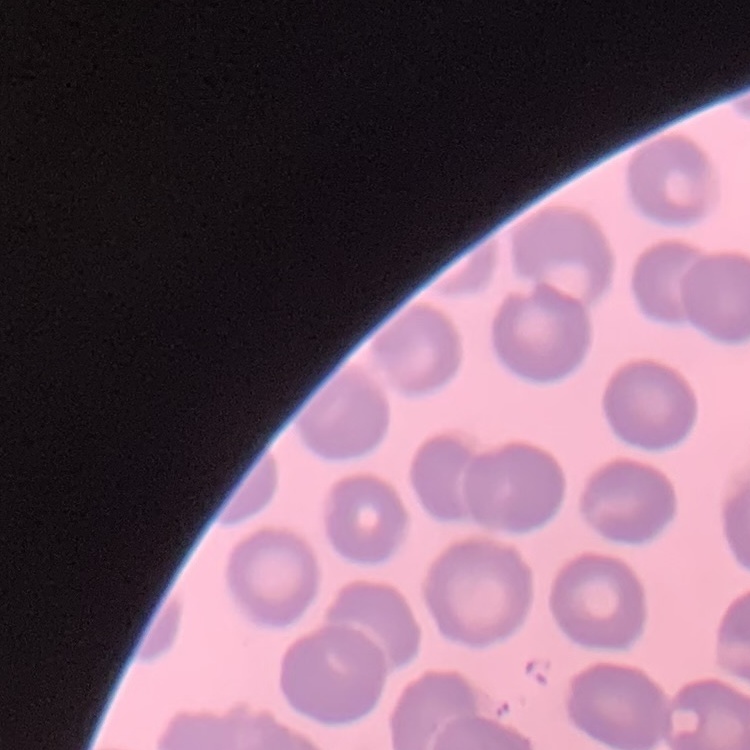

Summary:
  - Red blood cell morphology: no rouleaux formation
  - Stain: Field's or Giemsa
  - Image type: square crop of a larger photomicrograph
  - Preparation: thin blood film